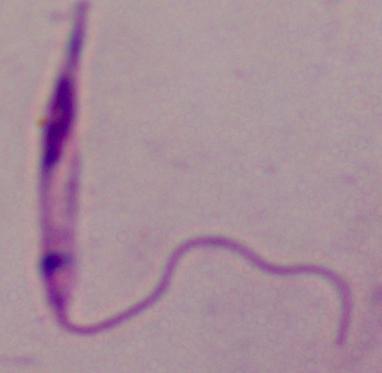 A Leishmania parasite is seen. 1000x magnification. Photomicrograph.